Identify the blood parasite species.
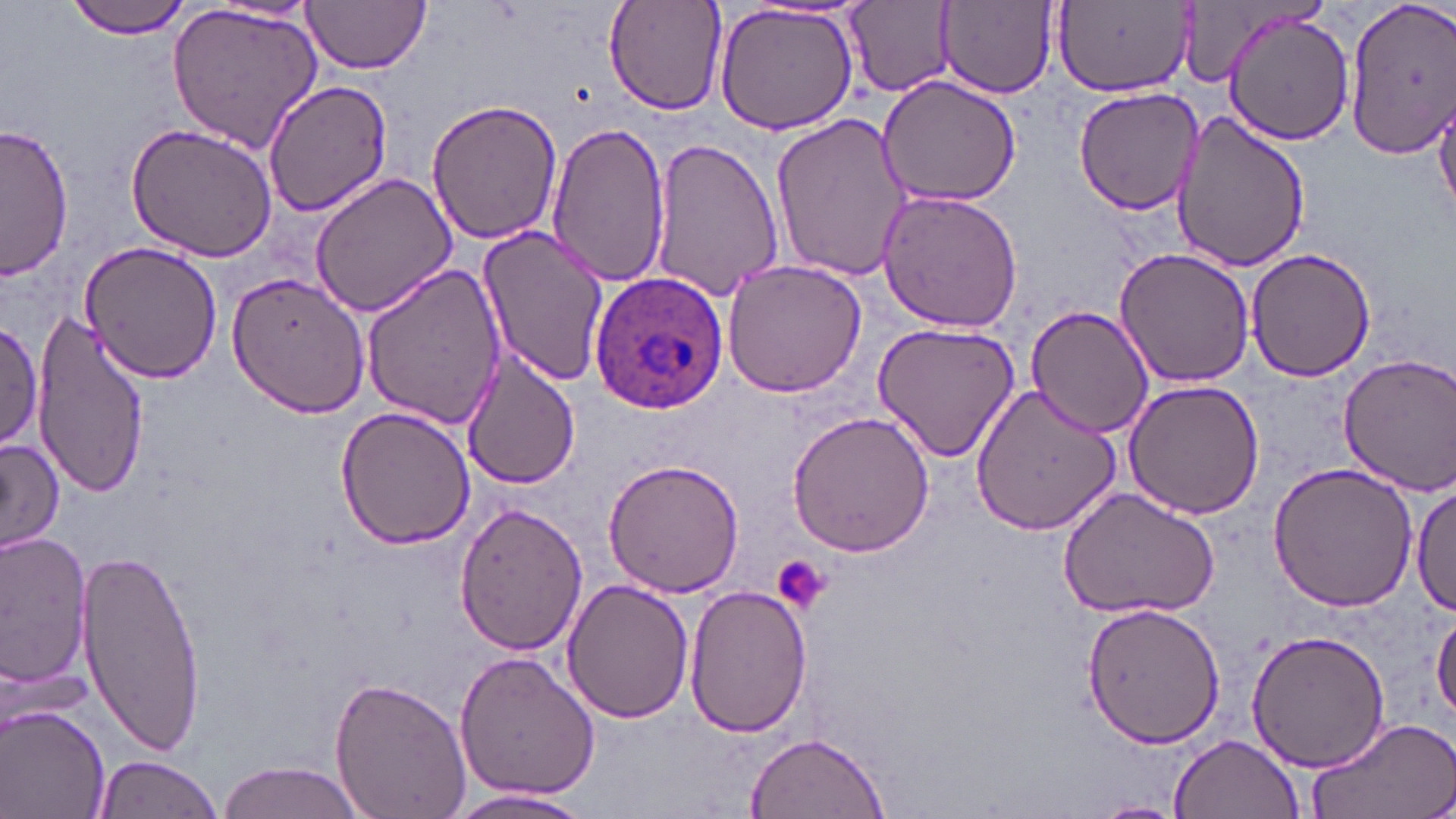

Plasmodium ovale.

Approximate bounding boxes as [x1, y1, x2, y2] in pixels. Plasmodium ovale-infected red blood cell locations: [587, 270, 732, 413]. Platelet locations: [770, 555, 832, 616]. Uninfected red blood cell locations: [65, 0, 193, 39], [602, 0, 729, 117], [1342, 0, 1456, 158], [301, 1, 432, 74], [845, 1, 955, 95], [940, 1, 1058, 97], [164, 2, 325, 153], [204, 2, 319, 27], [711, 3, 861, 136], [1054, 4, 1193, 99], [1222, 12, 1358, 145], [876, 75, 1024, 207], [262, 79, 393, 217], [1072, 84, 1204, 215], [1436, 94, 1456, 222], [426, 97, 562, 246], [1171, 112, 1312, 273], [770, 113, 917, 281], [546, 120, 671, 288], [124, 122, 278, 262], [1, 123, 75, 280], [651, 137, 786, 300], [309, 172, 456, 317], [875, 186, 1027, 333], [476, 226, 607, 386], [78, 240, 223, 384], [1113, 247, 1255, 388], [1245, 247, 1379, 381], [721, 259, 870, 399], [361, 265, 508, 429], [226, 270, 370, 418], [1025, 305, 1153, 437], [33, 308, 151, 495], [0, 318, 45, 453], [872, 319, 1021, 463], [459, 349, 580, 488], [1335, 354, 1456, 494], [1121, 380, 1267, 520], [972, 384, 1123, 536], [336, 403, 478, 550], [786, 411, 934, 557], [0, 435, 66, 556], [605, 456, 746, 598], [1266, 461, 1419, 613], [1412, 484, 1455, 618], [1058, 486, 1222, 620], [451, 502, 587, 656], [2, 531, 96, 691], [75, 542, 206, 754], [560, 579, 695, 724], [682, 585, 813, 739], [1083, 602, 1224, 748], [1432, 608, 1456, 725], [1246, 627, 1391, 772], [452, 650, 601, 805], [328, 676, 472, 819], [1, 705, 112, 819], [1304, 717, 1456, 819], [744, 731, 889, 818], [1168, 734, 1306, 819], [92, 756, 225, 819], [215, 761, 370, 819], [446, 787, 597, 818], [1085, 800, 1188, 819]. Single field of view. May-Grünwald-Giemsa-stained preparation. Thin blood smear. Image is 1456×819 pixels. Captured at 1000x magnification. Optical microscopy.